Describe the morphology of the red blood cells.
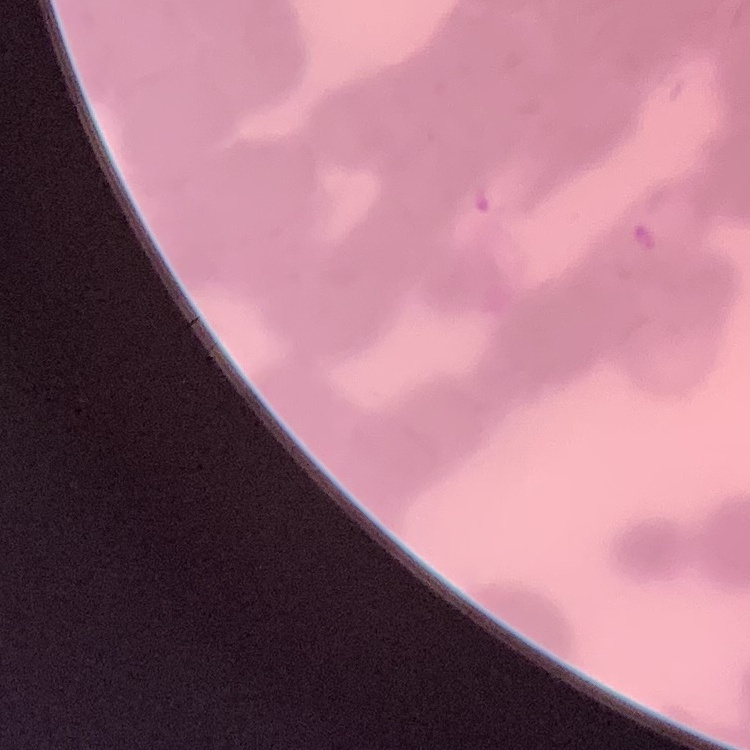

They show rouleaux formation.

image type = one tile cut from a larger photomicrograph
stain = Field's or Giemsa
preparation = thin blood film